Identify the cell.
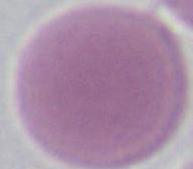
An erythrocyte.

Summary:
  - Modality: micrograph
  - Magnification: 1000x